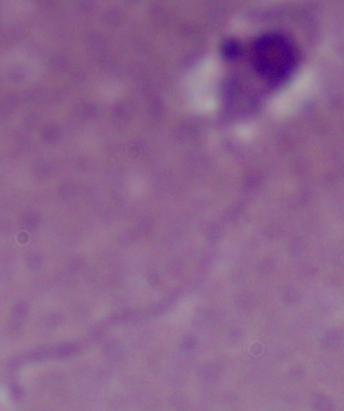 A Leishmania parasite is shown. Captured at 1000x magnification. Micrograph.